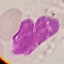
Summary:
  - Malaria status: uninfected
  - Capture: smartphone through the microscope eyepiece
  - Preparation: thin smear
  - Stain: Giemsa
  - Image type: cell patch, automatically extracted from a larger field of view and resized to 64 × 64 pixels